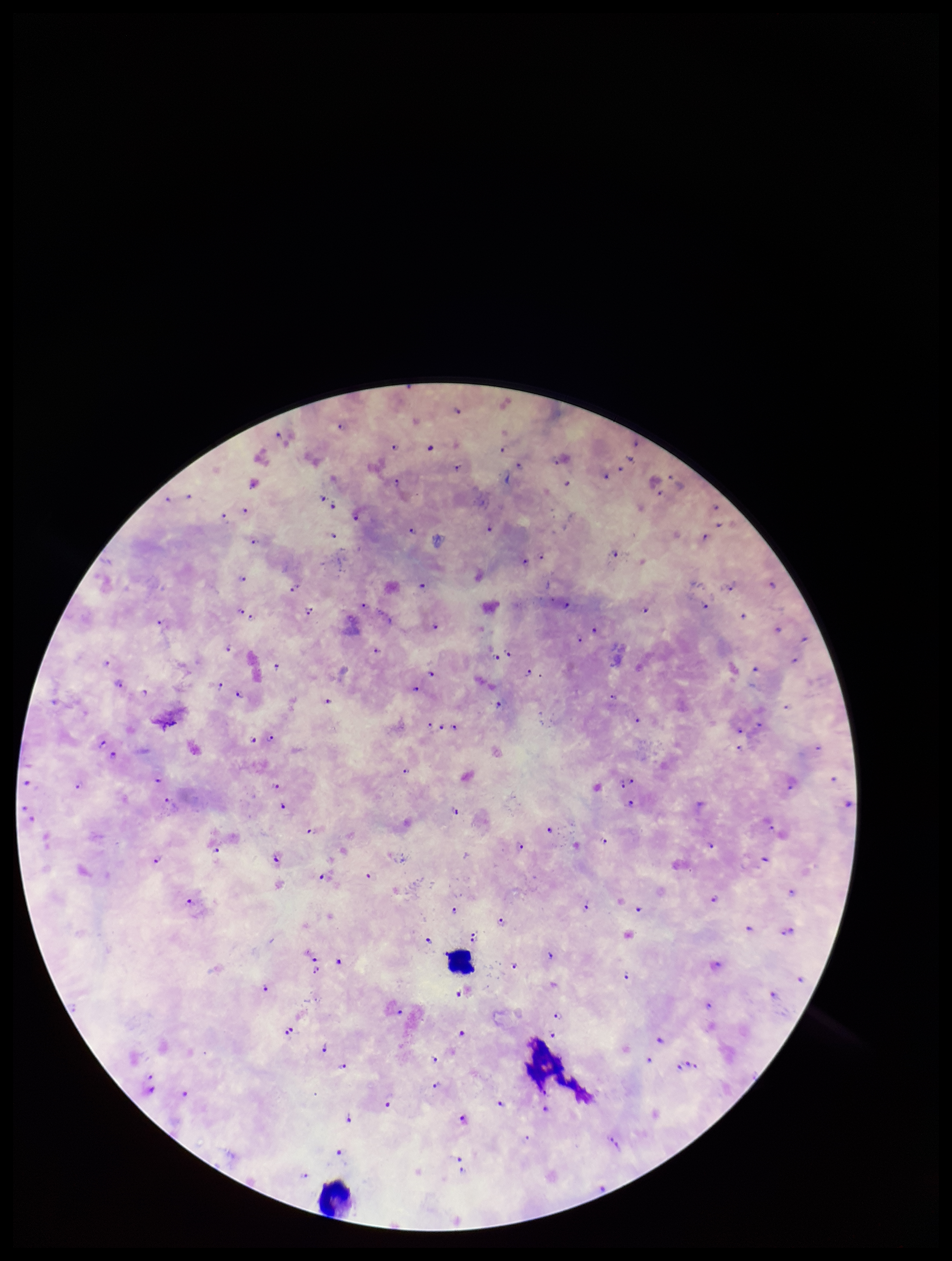

Plasmodium parasites = detected
parasite count = 119
patient malaria status = positive
field of view = one from this slide
preparation = thick
leukocyte count = 2
capture = smartphone photograph through the microscope eyepiece
species reported for this patient = Plasmodium falciparum
stain = Giemsa
image size = 952×1261 pixels